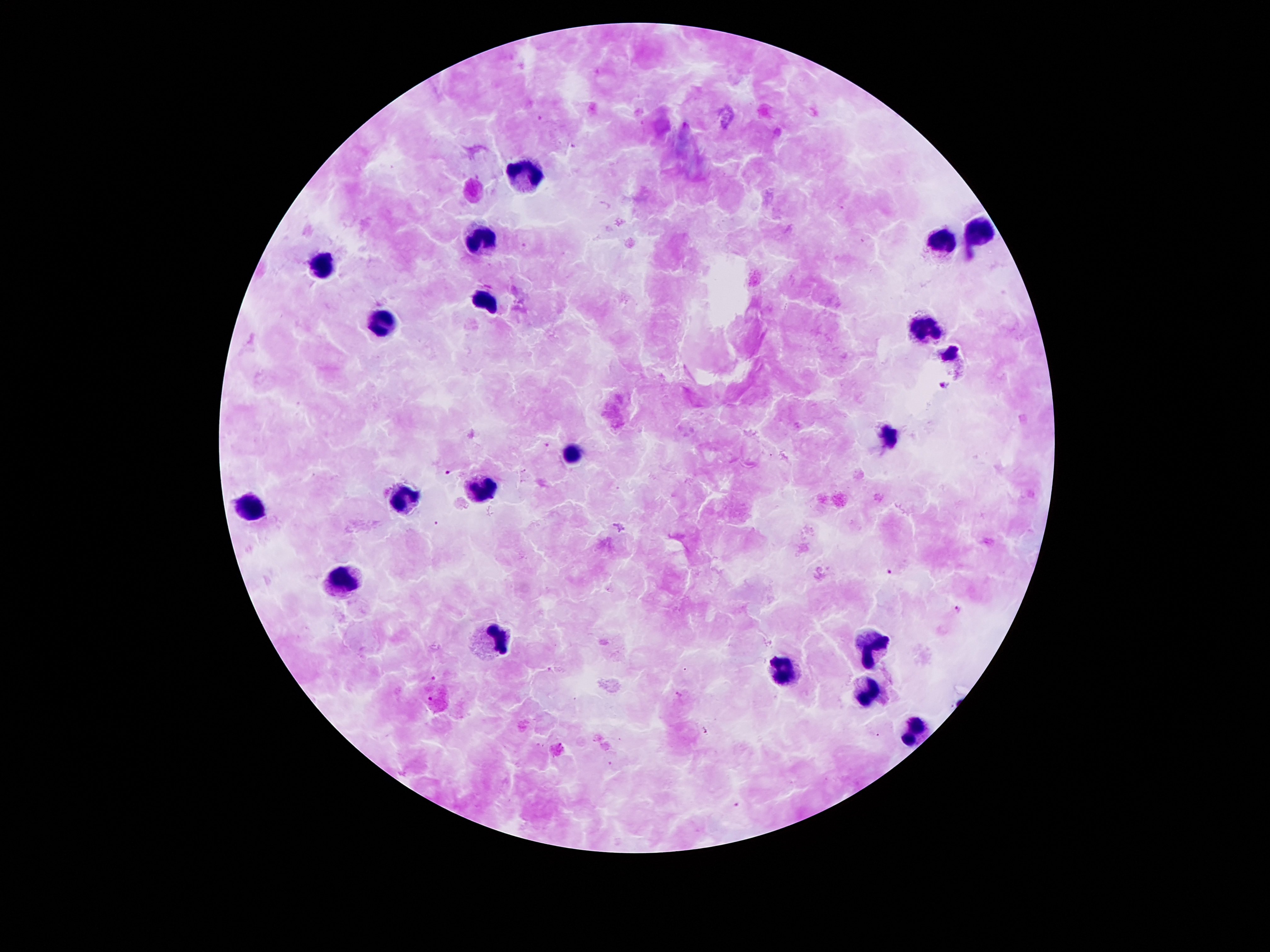

Approximate object centers, in pixels from the top-left corner. Leukocyte locations: (x=520, y=176), (x=978, y=232), (x=940, y=240), (x=479, y=243), (x=321, y=261), (x=486, y=299), (x=386, y=324), (x=928, y=327), (x=947, y=353), (x=890, y=436), (x=573, y=460), (x=483, y=491), (x=402, y=498), (x=246, y=504), (x=339, y=581), (x=495, y=640), (x=872, y=643), (x=785, y=674), (x=862, y=688), (x=912, y=727). Plasmodium parasite locations: (x=943, y=387), (x=548, y=446), (x=447, y=472), (x=436, y=522), (x=890, y=573), (x=957, y=608), (x=433, y=678), (x=432, y=698), (x=736, y=805). Smartphone photograph taken through the microscope eyepiece. Thick blood film. Patient malaria status: infected with Plasmodium falciparum. 100x magnification. Giemsa stain. Image is 1270×952 pixels. Single field of view.